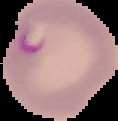
Cell region segmented out of the field of view; the surrounding area is masked to black. From a thin blood smear. Result: Plasmodium parasites identified. Image is 118×121 pixels.